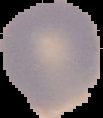

result = no malaria parasites detected
image type = cell region segmented out of the field of view; surrounding area masked to black
image size = 103×118 pixels
preparation = thin blood film